Name the blood parasite species.
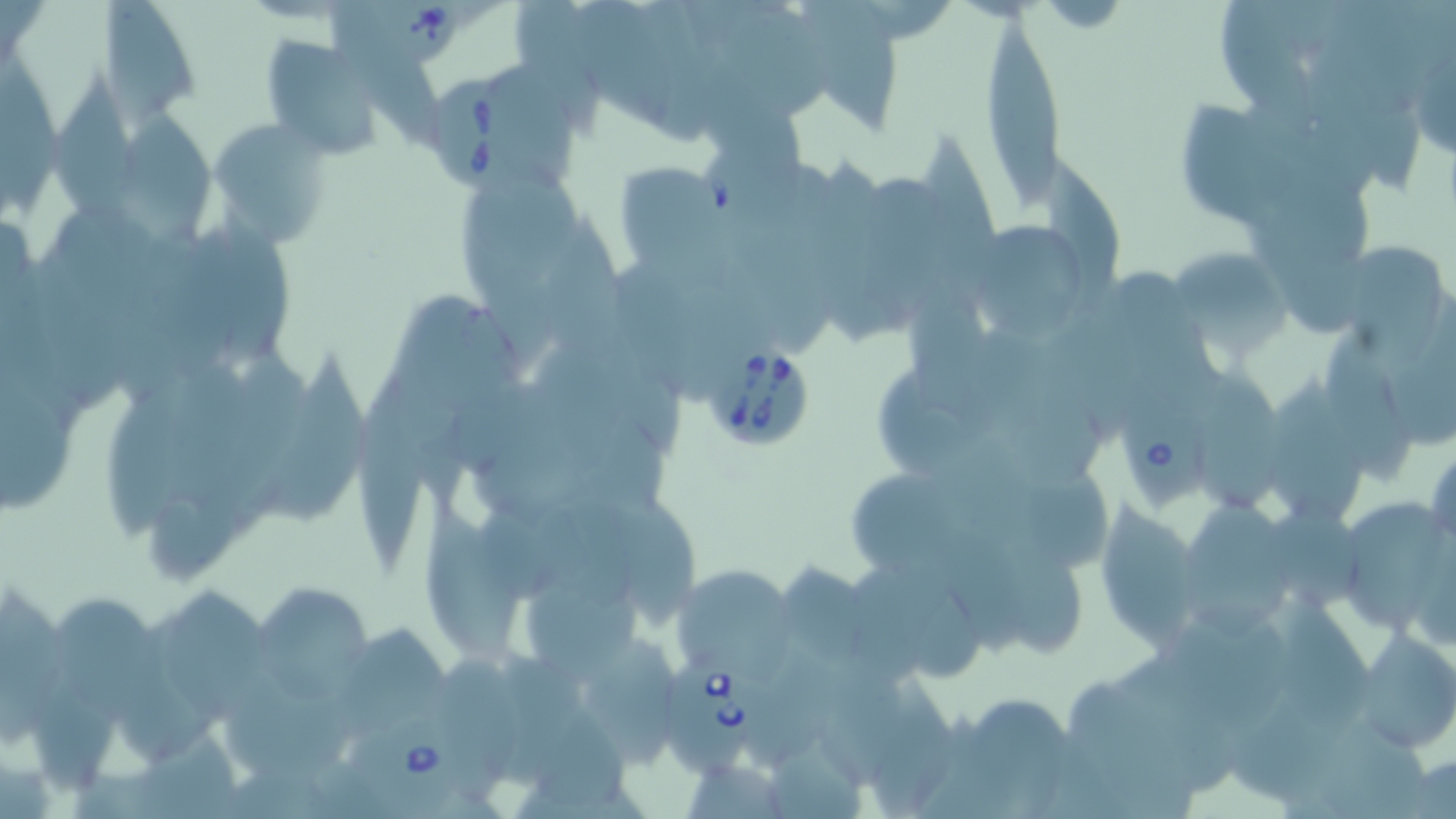
Babesia divergens.

image_size: 1456×819 pixels
babesia_divergens_infected_red_blood_cell_locations: 'approximate bounding boxes as named x1/y1/x2/y2 corners in pixels: (x1=351, y1=0, x2=461, y2=69), (x1=436, y1=73, x2=539, y2=189), (x1=706, y1=343, x2=814, y2=451), (x1=1114, y1=391, x2=1211, y2=512), (x1=659, y1=655, x2=764, y2=777), (x1=346, y1=714, x2=471, y2=809)'
preparation: thin blood smear
uninfected_red_blood_cell_locations: 'approximate bounding boxes as named x1/y1/x2/y2 corners in pixels: (x1=98, y1=0, x2=205, y2=122), (x1=576, y1=0, x2=673, y2=128), (x1=804, y1=0, x2=901, y2=144), (x1=1222, y1=1, x2=1317, y2=134), (x1=518, y1=2, x2=602, y2=138), (x1=730, y1=7, x2=835, y2=118), (x1=977, y1=14, x2=1067, y2=212), (x1=258, y1=36, x2=387, y2=159), (x1=338, y1=39, x2=440, y2=151), (x1=1406, y1=41, x2=1456, y2=163), (x1=0, y1=46, x2=60, y2=218), (x1=495, y1=61, x2=574, y2=176), (x1=54, y1=75, x2=140, y2=218), (x1=700, y1=75, x2=808, y2=205), (x1=1180, y1=94, x2=1272, y2=228), (x1=129, y1=107, x2=213, y2=241), (x1=210, y1=121, x2=332, y2=244), (x1=919, y1=124, x2=995, y2=278), (x1=1045, y1=156, x2=1119, y2=295), (x1=610, y1=160, x2=725, y2=268), (x1=465, y1=166, x2=588, y2=267), (x1=867, y1=178, x2=949, y2=317), (x1=59, y1=208, x2=163, y2=302), (x1=206, y1=210, x2=298, y2=363), (x1=549, y1=218, x2=633, y2=358), (x1=972, y1=225, x2=1090, y2=344), (x1=1274, y1=238, x2=1367, y2=336), (x1=1345, y1=239, x2=1440, y2=366), (x1=1169, y1=247, x2=1297, y2=357), (x1=1377, y1=285, x2=1456, y2=454), (x1=403, y1=291, x2=525, y2=408), (x1=1328, y1=334, x2=1417, y2=484), (x1=1199, y1=343, x2=1281, y2=511), (x1=273, y1=346, x2=366, y2=521), (x1=222, y1=350, x2=304, y2=504), (x1=161, y1=361, x2=248, y2=516), (x1=1, y1=366, x2=72, y2=515), (x1=879, y1=368, x2=979, y2=477), (x1=1272, y1=373, x2=1359, y2=524), (x1=358, y1=378, x2=428, y2=570), (x1=100, y1=381, x2=193, y2=539), (x1=1000, y1=384, x2=1102, y2=490), (x1=1426, y1=440, x2=1455, y2=555), (x1=853, y1=473, x2=950, y2=568), (x1=1188, y1=491, x2=1291, y2=636), (x1=1270, y1=491, x2=1363, y2=607), (x1=1336, y1=494, x2=1453, y2=637), (x1=152, y1=496, x2=228, y2=572), (x1=623, y1=496, x2=697, y2=628), (x1=1093, y1=498, x2=1206, y2=650), (x1=424, y1=506, x2=524, y2=656), (x1=1001, y1=531, x2=1086, y2=655), (x1=937, y1=533, x2=1037, y2=663), (x1=782, y1=564, x2=867, y2=668), (x1=676, y1=566, x2=791, y2=668), (x1=864, y1=567, x2=980, y2=677), (x1=525, y1=577, x2=643, y2=678), (x1=166, y1=585, x2=268, y2=714), (x1=252, y1=585, x2=379, y2=701), (x1=0, y1=586, x2=59, y2=741), (x1=55, y1=593, x2=169, y2=717), (x1=1277, y1=596, x2=1378, y2=732), (x1=1177, y1=605, x2=1310, y2=731), (x1=334, y1=624, x2=450, y2=736), (x1=1349, y1=629, x2=1456, y2=754), (x1=584, y1=635, x2=679, y2=768), (x1=502, y1=652, x2=579, y2=783), (x1=828, y1=653, x2=909, y2=792), (x1=759, y1=655, x2=834, y2=764), (x1=439, y1=656, x2=524, y2=782), (x1=1067, y1=678, x2=1196, y2=819), (x1=222, y1=685, x2=360, y2=779), (x1=971, y1=690, x2=1070, y2=815), (x1=541, y1=715, x2=629, y2=809), (x1=773, y1=752, x2=864, y2=819), (x1=690, y1=762, x2=782, y2=819)'
field_of_view: single
magnification: 1000x
stain: May-Grünwald-Giemsa
modality: light microscopy